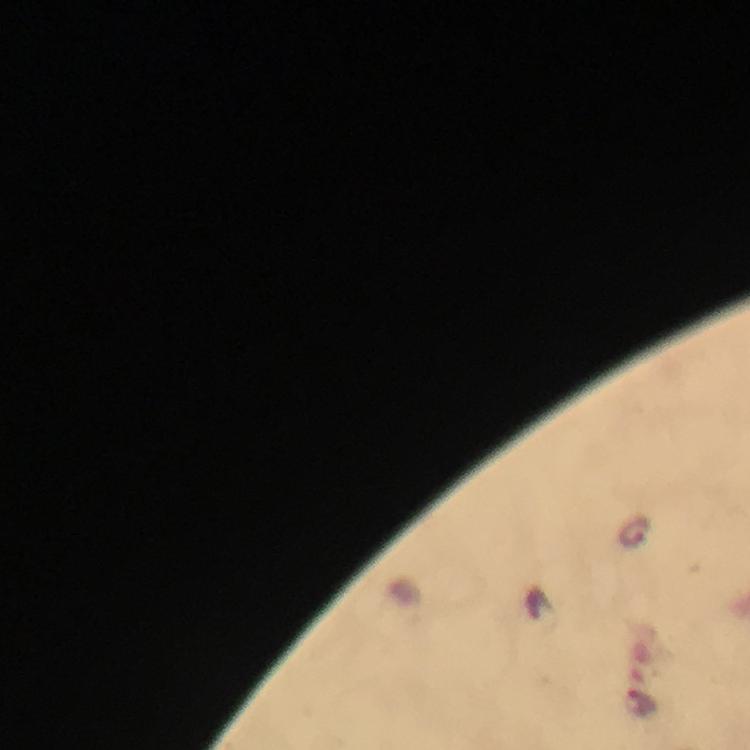

preparation = thick smear
magnification = 100x
stain = Giemsa
capture = smartphone mounted on the microscope
context = from a diagnostic examination for malaria
immersion oil = used
malaria parasite locations = approximate centers as {x, y} in pixels: {635, 533}, {638, 702}
cropped from = a single field of view
image size = 750×750 pixels